Identify the parasite.
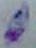

Toxoplasma gondii.

{
  "modality": "micrograph",
  "magnification": "1000x"
}